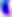
identification: Toxoplasma gondii
magnification: 400x
modality: micrograph